Classify this cell by malaria status.
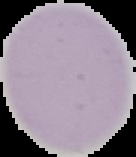

It is uninfected.

Image is 136×157 pixels. From a thin blood film. Segmented cell region on a black background.